Locate and identify every blood parasite.
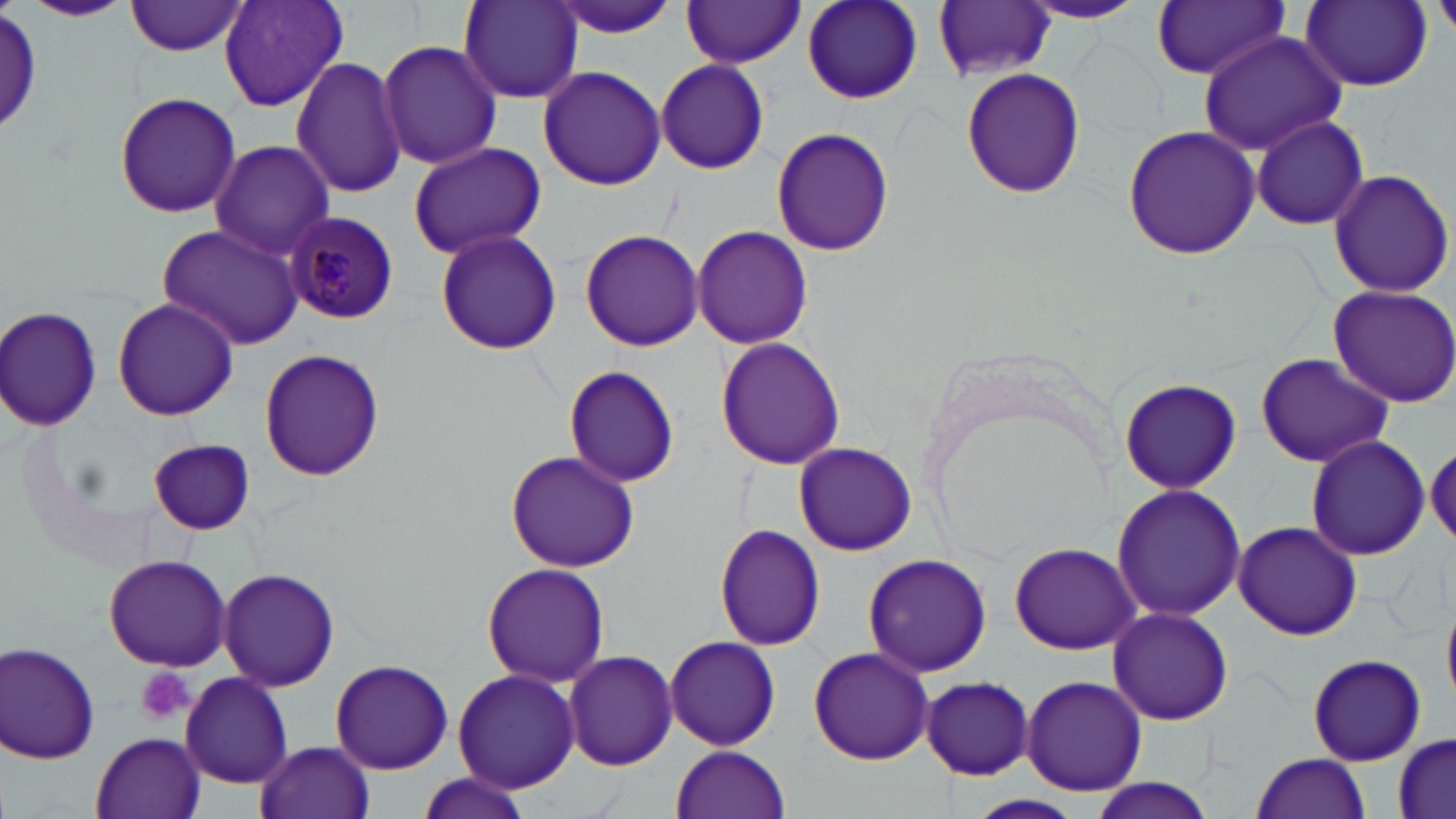
Approximate bounding boxes as (x1, y1, x2, y2) in pixels.
Plasmodium malariae-infected red blood cells: (285, 212, 399, 324).
No Plasmodium falciparum, Plasmodium ovale, Plasmodium vivax, Babesia divergens, or Trypanosoma brucei observed.

Summary:
  - Uninfected red blood cell locations: (126, 0, 248, 57), (217, 0, 350, 113), (803, 0, 923, 105), (1301, 0, 1432, 90), (25, 1, 133, 22), (458, 1, 582, 103), (547, 1, 681, 41), (680, 1, 806, 67), (1020, 1, 1149, 24), (1153, 1, 1290, 79), (935, 3, 1057, 82), (1, 7, 44, 137), (1199, 31, 1348, 156), (377, 40, 502, 171), (289, 56, 408, 199), (656, 60, 768, 174), (538, 65, 666, 191), (961, 67, 1086, 197), (115, 93, 241, 218), (1251, 115, 1369, 230), (1121, 124, 1260, 260), (771, 127, 894, 255), (209, 140, 335, 259), (407, 141, 548, 260), (1325, 169, 1454, 298), (156, 223, 305, 350), (692, 224, 813, 350), (434, 227, 562, 356), (579, 228, 703, 352), (1326, 285, 1456, 407), (112, 298, 239, 420), (0, 304, 102, 430), (715, 336, 846, 469), (257, 347, 384, 479), (1254, 352, 1395, 467), (562, 363, 679, 488), (1118, 376, 1244, 492), (1304, 433, 1429, 561), (1427, 438, 1456, 549), (148, 439, 254, 534), (794, 443, 916, 555), (505, 449, 640, 572), (1110, 483, 1247, 621), (1233, 520, 1362, 640), (714, 524, 827, 651), (1009, 541, 1140, 655), (861, 552, 992, 677), (104, 554, 231, 670), (482, 563, 612, 690), (220, 568, 339, 691), (1106, 607, 1234, 725), (663, 635, 780, 751), (1, 642, 101, 763), (808, 644, 936, 765), (562, 649, 679, 772), (1306, 654, 1426, 765), (331, 659, 453, 775), (452, 668, 581, 792), (180, 671, 293, 788), (1020, 675, 1147, 795), (921, 676, 1034, 778), (91, 732, 205, 819), (1392, 734, 1454, 819), (255, 740, 375, 819), (670, 745, 790, 819), (1251, 753, 1373, 819), (415, 775, 535, 819), (1078, 779, 1221, 818)
  - Platelet locations: (135, 665, 194, 725)
  - Slide-level diagnosis: Plasmodium malariae
  - Image size: 1456×819 pixels
  - Modality: optical microscopy
  - Stain: May-Grünwald-Giemsa
  - Magnification: 1000x
  - Field of view: single
  - Preparation: thin blood film